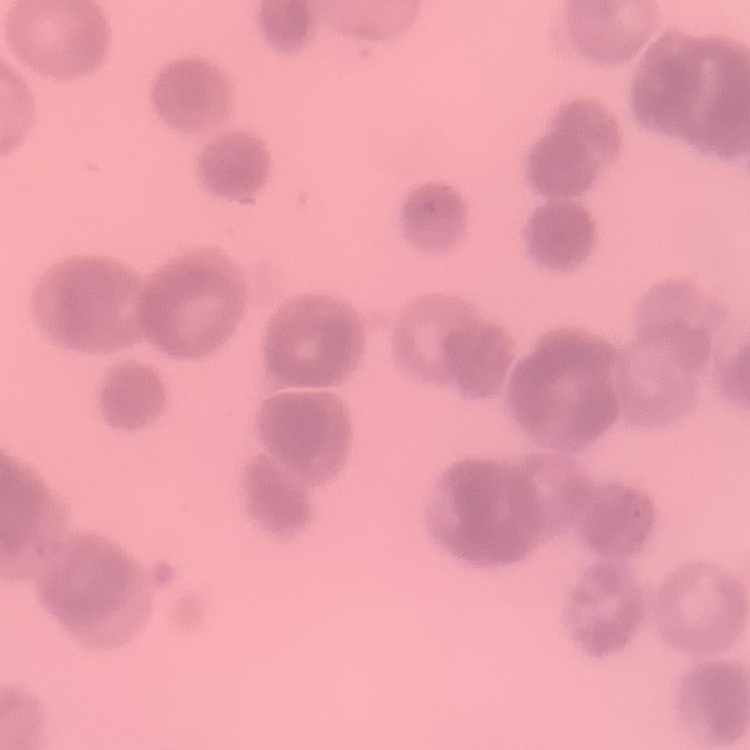

The erythrocytes exhibit rouleaux formation. Stained with either Field's or Giemsa. Thin peripheral smear. One tile cut from a larger photomicrograph.